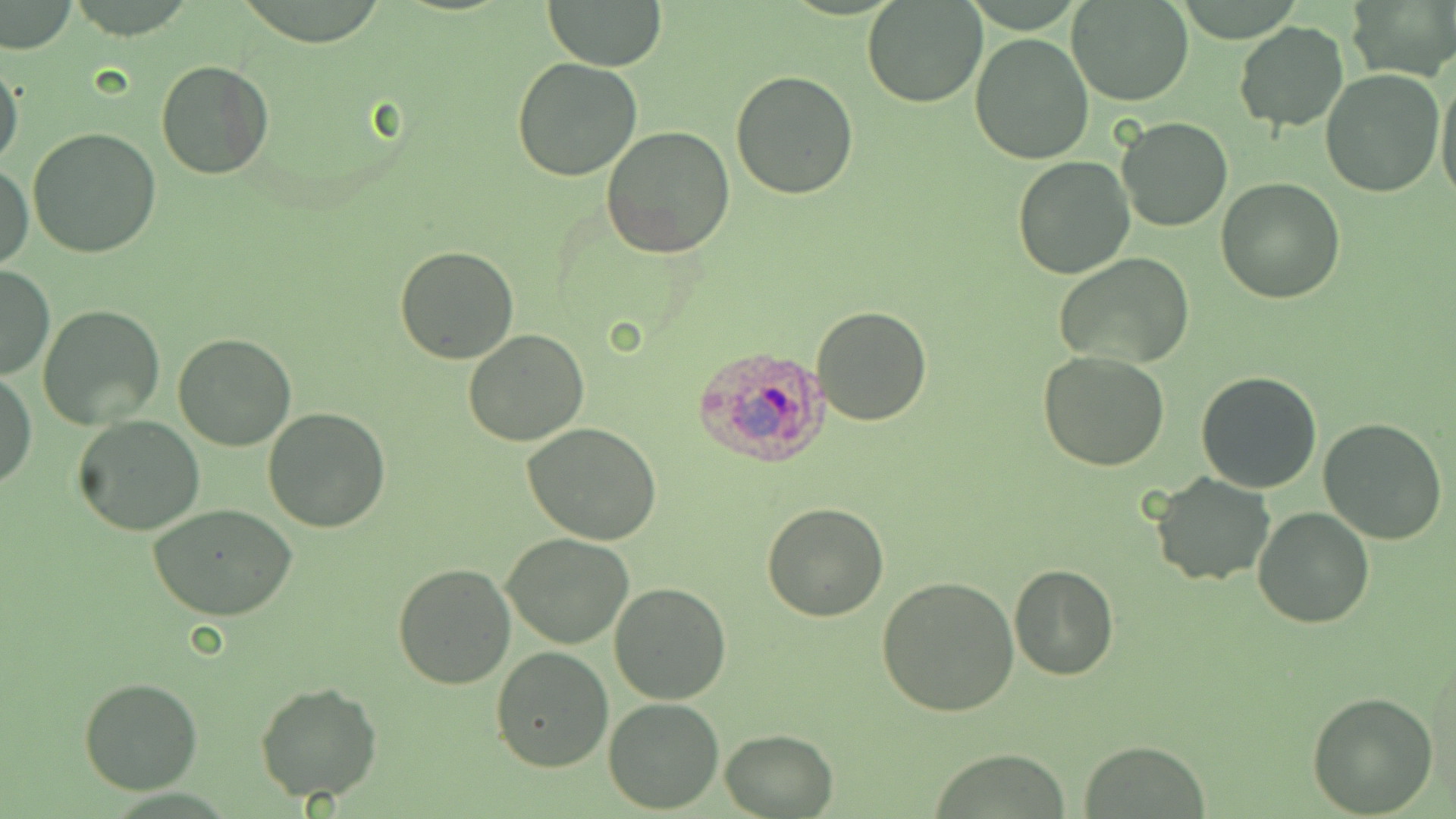

Approximate bounding boxes as (x1,y1)-(x2,y2) corner pairs in pixels. Plasmodium ovale-infected red blood cell locations: (690,344)-(831,467). Uninfected red blood cell locations: (542,0)-(668,70), (862,0)-(986,107), (1068,0)-(1194,106), (0,2)-(79,55), (1344,3)-(1456,79), (1232,21)-(1351,132), (969,31)-(1094,165), (0,54)-(24,175), (511,57)-(643,181), (155,60)-(275,180), (730,68)-(859,198), (1319,69)-(1445,198), (1435,70)-(1456,207), (1116,117)-(1233,232), (27,127)-(161,260), (602,127)-(736,261), (1012,156)-(1136,279), (0,162)-(34,270), (1216,178)-(1345,303), (395,244)-(522,365), (1054,252)-(1196,370), (1,265)-(53,380), (37,304)-(167,428), (810,306)-(932,427), (463,328)-(590,446), (174,333)-(296,451), (1038,351)-(1171,472), (0,369)-(36,493), (1196,372)-(1324,493), (262,408)-(391,533), (72,415)-(205,535), (1318,418)-(1447,545), (521,421)-(665,547), (1151,473)-(1274,587), (762,502)-(891,622), (147,504)-(298,622), (1254,508)-(1373,628), (502,532)-(635,649), (392,564)-(515,689), (1009,564)-(1117,679), (875,576)-(1020,715), (608,581)-(731,704), (491,646)-(614,772), (78,676)-(203,795), (255,681)-(383,804), (1306,691)-(1438,815), (604,698)-(724,813), (721,729)-(837,817), (1080,740)-(1211,817), (929,748)-(1073,818). Slide-level diagnosis: Plasmodium ovale. One field of a larger specimen. Thin blood smear. May-Grünwald-Giemsa-stained preparation. Optical microscopy. 1000x magnification. Image is 1456×819 pixels.